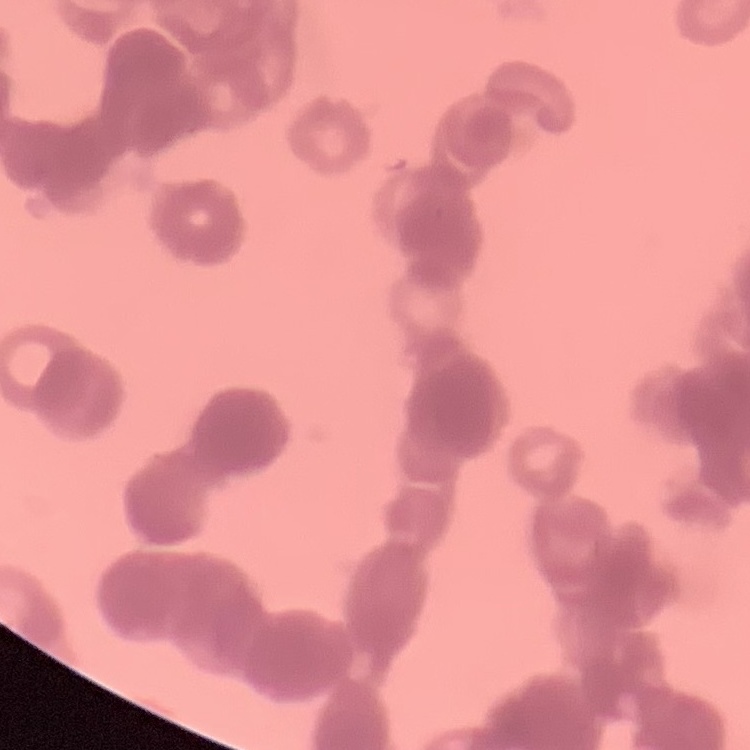

The erythrocytes exhibit rouleaux formation. Thin peripheral smear. One tile cut from a larger photomicrograph. Field's or Giemsa stain.